Assess the morphology of the red blood cells.
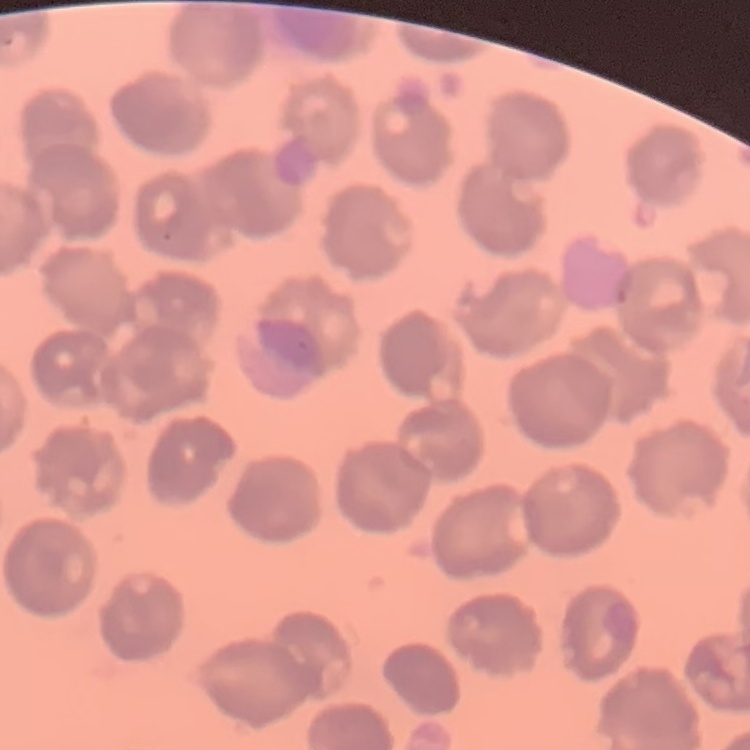
They show no rouleaux formation.

Field's or Giemsa stain. Thin blood smear. One tile cut from a larger photomicrograph.